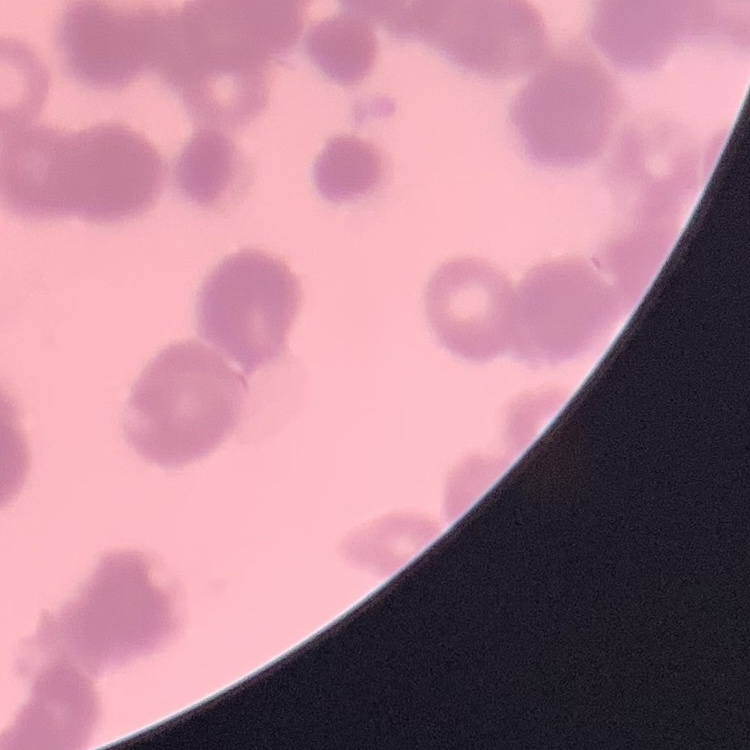
The erythrocytes show rouleaux formation. Thin blood smear. Square crop of a larger photomicrograph. Field's or Giemsa stain.